Report the malaria status of this cell.
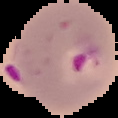

Parasitized.

preparation = thin blood film
image type = cell region segmented out of the field of view; surrounding area masked to black
image size = 118×118 pixels